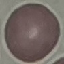

malaria_status: uninfected
image_type: cell patch, automatically extracted from a larger field of view and resized to 64 × 64 pixels
preparation: thin blood film
stain: Giemsa
capture: smartphone through the microscope eyepiece